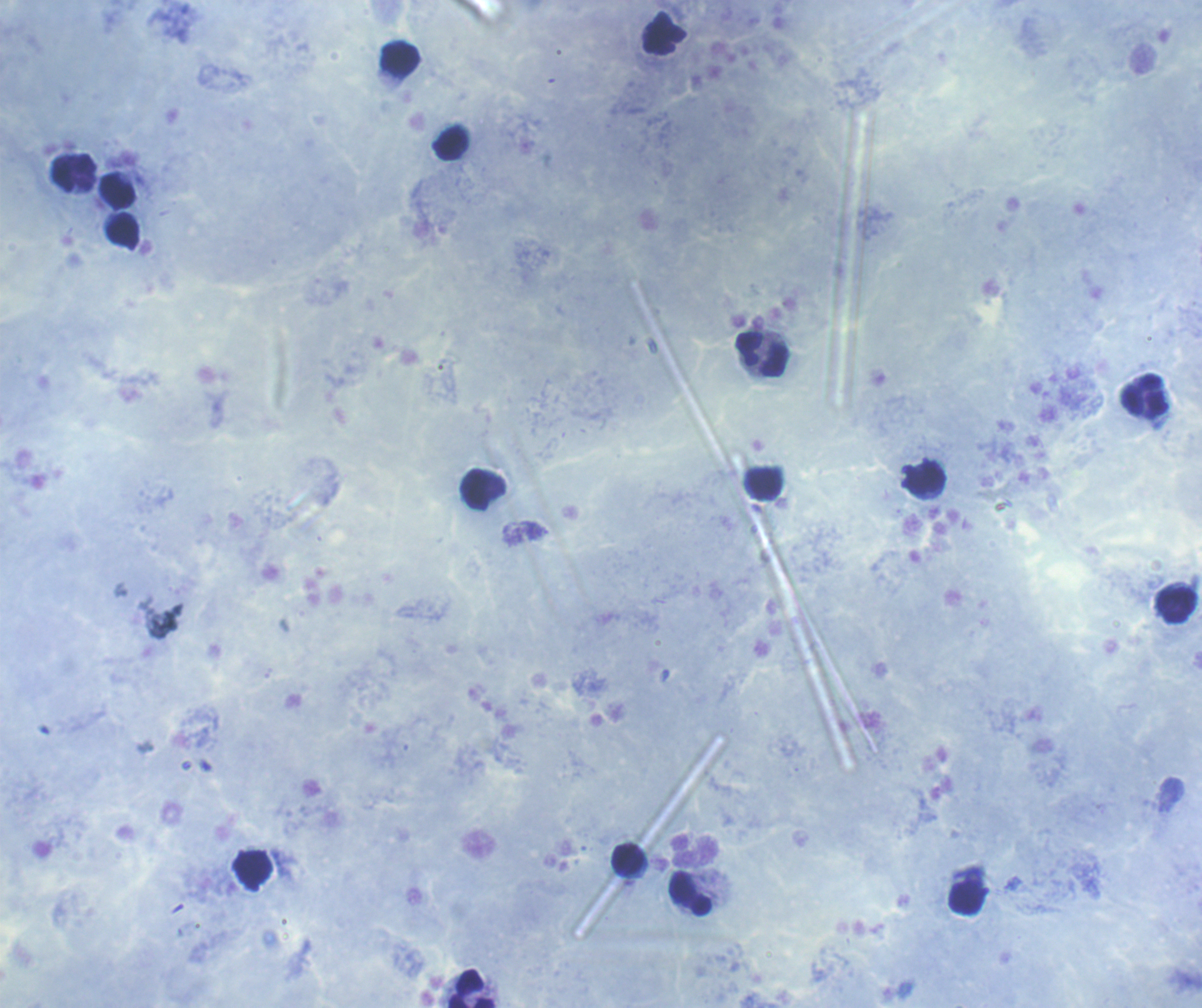
coordinate format = approximate centers as [x, y] in pixels
leukocyte locations = [400, 59], [450, 143], [73, 172], [118, 192], [124, 230], [761, 354], [1146, 395], [926, 479], [767, 483], [476, 489], [1176, 606], [627, 859], [253, 871], [690, 894], [967, 898], [472, 988]
preparation = thick blood smear
coloration quality = good
result = no Plasmodium parasites seen
magnification = 100x
image size = 1202×1008 pixels
background quality = satisfactory
stain = Romanowsky
field of view = one from this slide
context = previously used in an actual diagnosis